Name the blood parasite species.
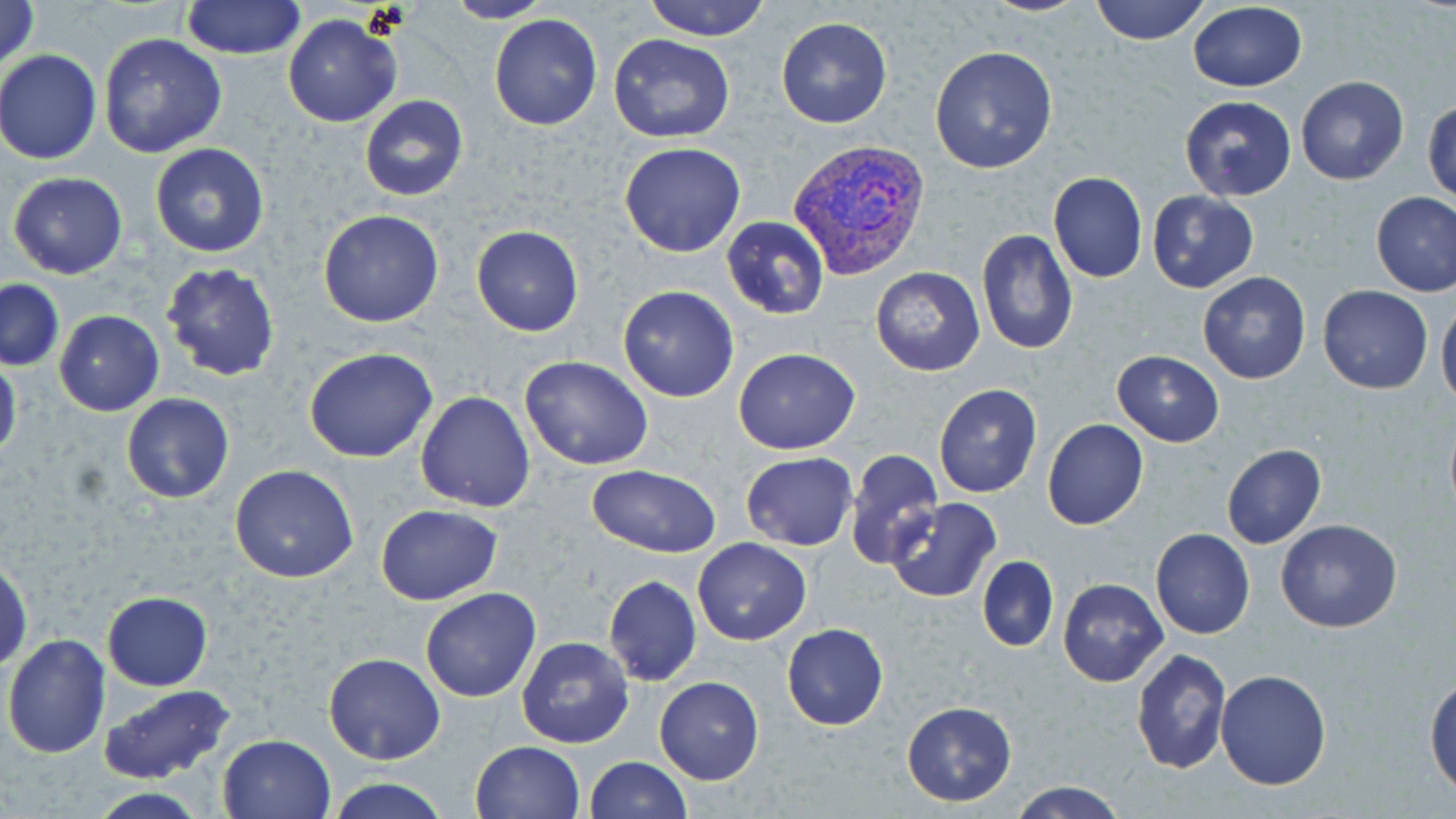
Plasmodium vivax.

{
  "image_size": "1456×819 pixels",
  "stain": "May-Grünwald-Giemsa",
  "plasmodium_vivax_infected_red_blood_cell_locations": "approximate bounding boxes as (x1, y1, x2, y2) in pixels: (790, 140, 929, 279)",
  "modality": "light microscopy",
  "preparation": "thin blood smear",
  "magnification": "1000x",
  "uninfected_red_blood_cell_locations": "approximate bounding boxes as (x1, y1, x2, y2) in pixels: (0, 0, 41, 78), (181, 0, 307, 61), (442, 0, 553, 24), (643, 0, 771, 41), (978, 0, 1092, 16), (1090, 0, 1211, 45), (1187, 4, 1308, 92), (489, 13, 602, 131), (282, 14, 402, 127), (775, 17, 892, 129), (98, 32, 227, 158), (608, 32, 736, 143), (929, 45, 1059, 172), (1, 49, 102, 165), (1295, 76, 1409, 186), (358, 95, 469, 201), (1179, 96, 1297, 201), (1424, 100, 1456, 204), (149, 142, 272, 258), (619, 142, 747, 257), (1048, 171, 1147, 283), (7, 172, 128, 279), (1147, 189, 1259, 293), (1371, 191, 1456, 297), (318, 208, 446, 328), (720, 216, 830, 321), (471, 224, 584, 337), (976, 229, 1078, 355), (160, 262, 281, 382), (871, 265, 984, 376), (1197, 271, 1312, 384), (1, 279, 64, 371), (618, 285, 740, 402), (1319, 285, 1434, 395), (1436, 298, 1456, 409), (54, 311, 163, 416), (304, 347, 438, 462), (732, 348, 860, 454), (1112, 350, 1225, 447), (520, 354, 655, 470), (0, 355, 22, 465), (933, 383, 1042, 498), (415, 391, 536, 512), (120, 394, 236, 506), (1041, 418, 1149, 531), (1221, 443, 1326, 548), (844, 448, 945, 571), (741, 452, 857, 550), (229, 464, 360, 583), (586, 465, 723, 559), (884, 496, 1001, 604), (374, 504, 503, 604), (1275, 519, 1403, 633), (1151, 529, 1256, 640), (693, 537, 812, 645), (977, 556, 1058, 650), (1, 559, 33, 672), (602, 576, 702, 685), (1057, 578, 1168, 686), (420, 588, 542, 701), (102, 593, 213, 689), (782, 623, 888, 731), (2, 634, 110, 759), (515, 636, 634, 749), (1130, 647, 1231, 775), (324, 652, 445, 764), (1215, 670, 1331, 791), (654, 676, 764, 784), (1425, 677, 1456, 798), (98, 684, 237, 783), (901, 701, 1017, 805), (217, 733, 335, 818), (469, 740, 584, 819), (584, 756, 691, 819), (327, 777, 450, 819), (1009, 780, 1128, 818), (88, 788, 213, 819)",
  "field_of_view": "one of a larger specimen"
}